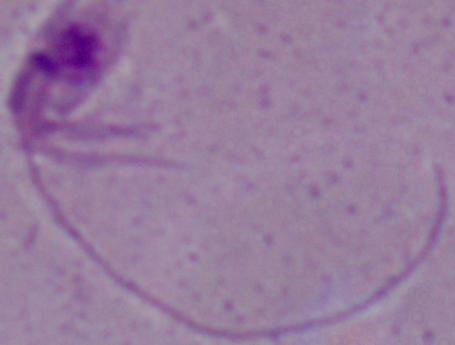

identification = Leishmania
magnification = 1000x
modality = micrograph